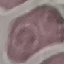
Result: no malaria parasites detected. Thin smear of blood. Automatically extracted cell patch, resized to 64 × 64 pixels. Acquired by smartphone through the microscope eyepiece. Giemsa stain.